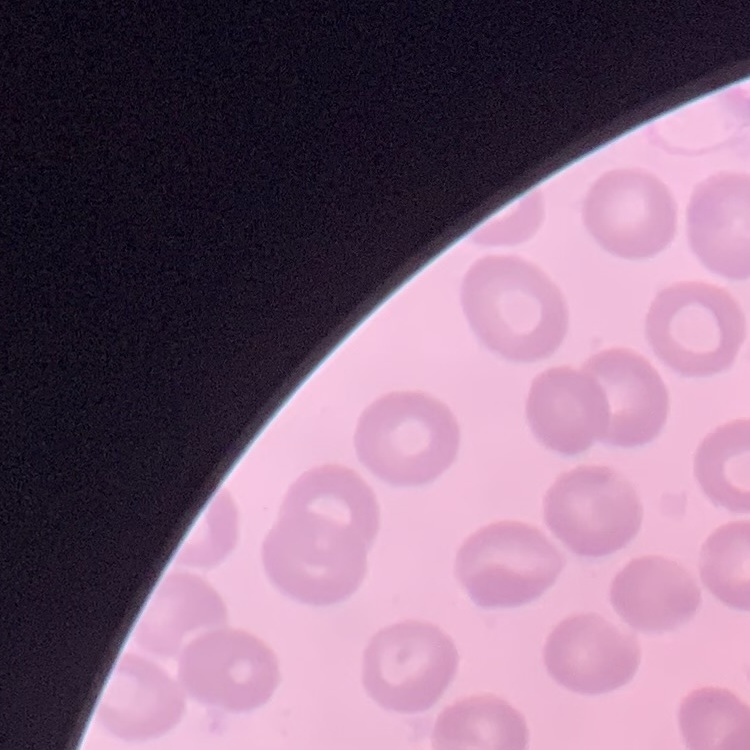 The erythrocytes show no rouleaux formation. Stained with either Field's or Giemsa. Square crop of a larger photomicrograph. Thin blood smear.